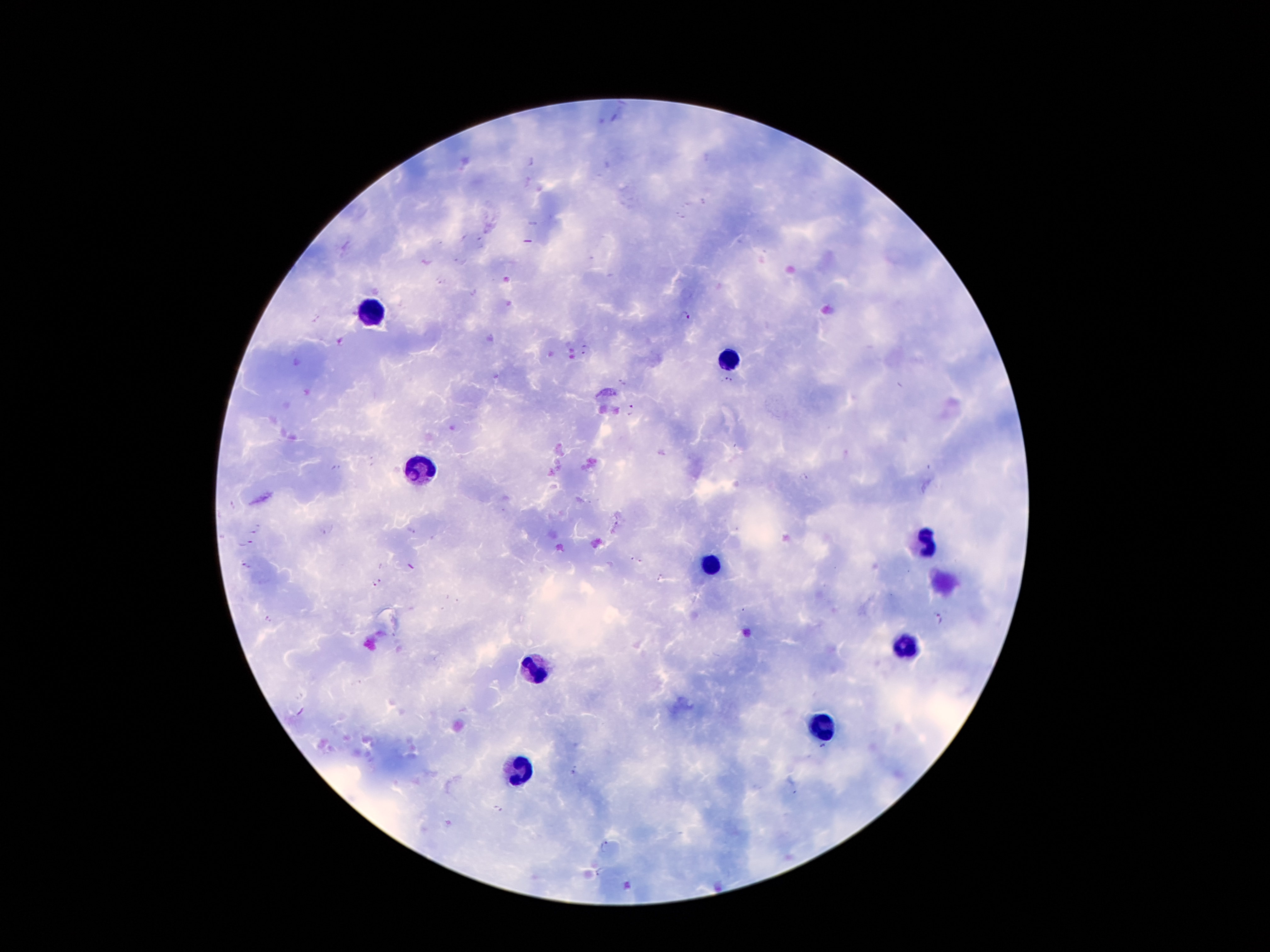
leukocyte_locations: 'approximate centers as {x, y} in pixels: {375, 312}, {728, 356}, {421, 465}, {921, 543}, {711, 562}, {906, 646}, {535, 669}, {824, 725}, {524, 772}'
preparation: thick blood film
patient_malaria_status: positive for Plasmodium falciparum
magnification: 100x
plasmodium_parasite_locations: 'approximate centers as {x, y} in pixels: {531, 161}, {702, 202}, {680, 216}, {463, 236}, {481, 243}, {591, 258}, {459, 263}, {441, 282}, {685, 315}, {585, 349}, {726, 379}, {623, 383}, {632, 410}, {804, 477}, {232, 505}, {254, 528}, {329, 529}, {412, 530}, {245, 544}, {631, 559}, {641, 561}, {245, 564}, {410, 567}, {661, 577}, {377, 583}, {268, 618}, {939, 618}, {355, 683}, {300, 696}, {823, 748}, {576, 768}, {497, 809}, {604, 846}, {598, 872}'
image_size: 1270×952 pixels
capture: smartphone camera through the microscope eyepiece
stain: Giemsa
field_of_view: single